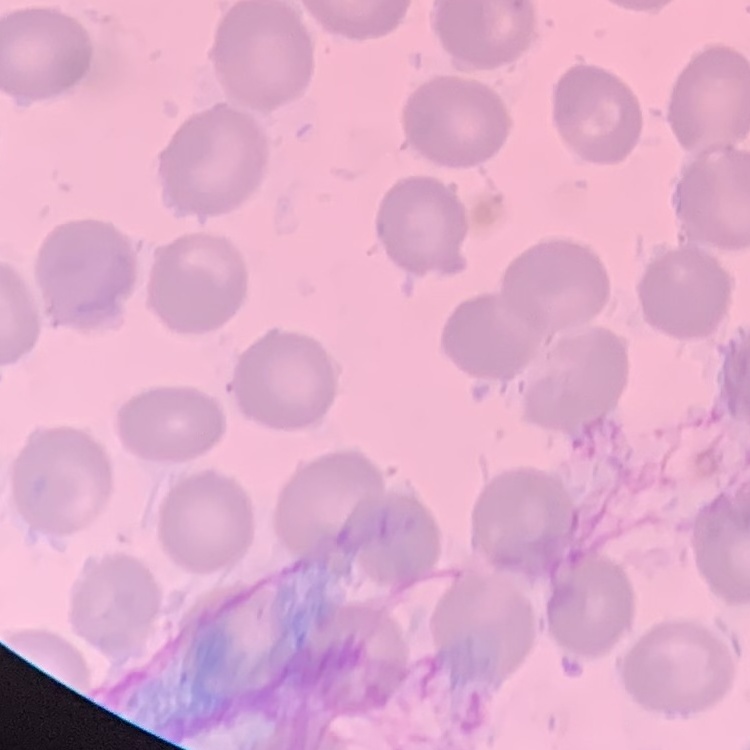
The red blood cells show no rouleaux formation. Stained with either Field's or Giemsa. Thin blood film. Square crop of a larger photomicrograph.